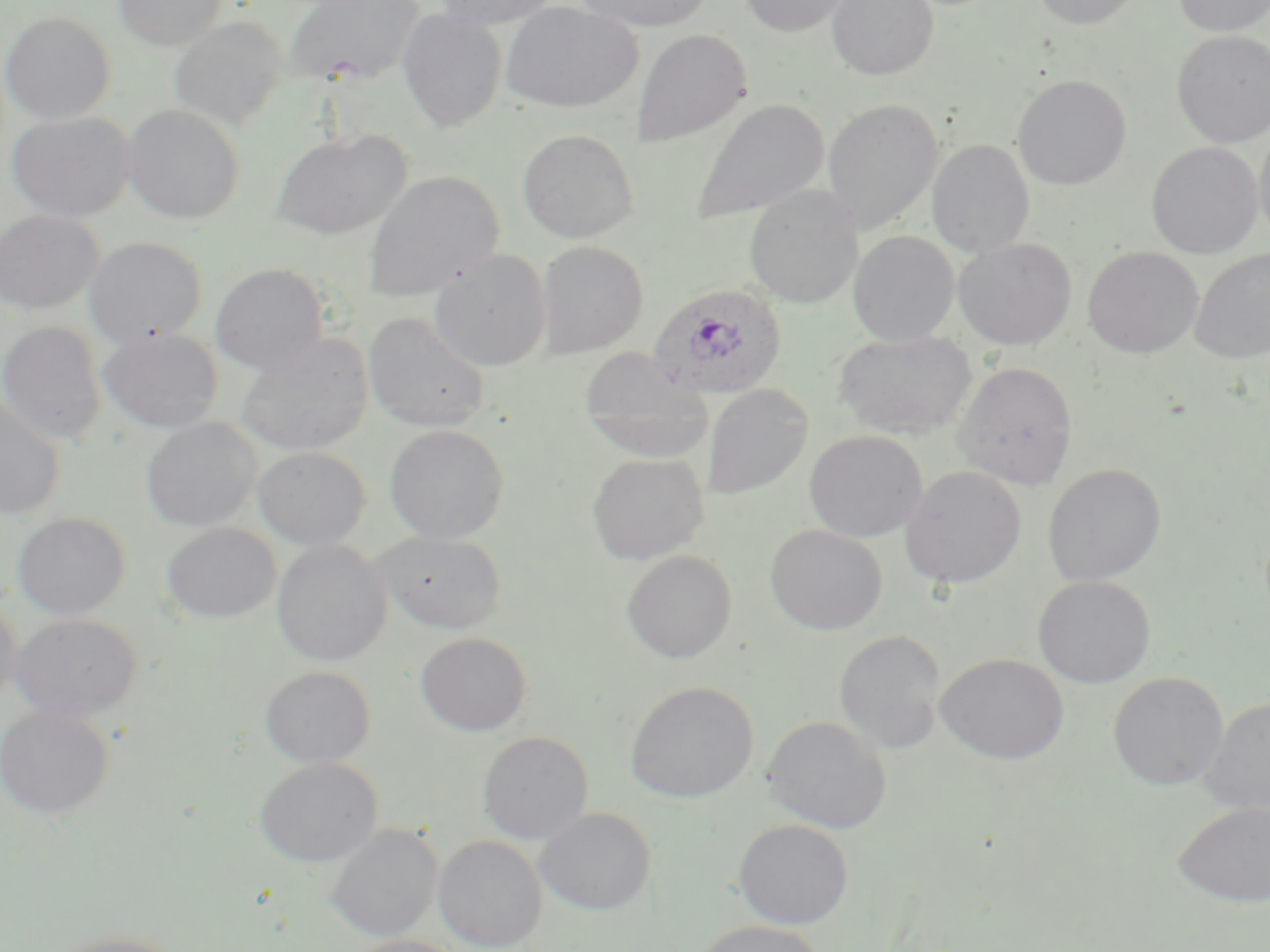

Summary:
  - Coordinate format: approximate bounding boxes as (x1, y1, x2, y2) in pixels
  - Plasmodium ovale-infected red blood cell locations: (648, 283, 788, 400)
  - Uninfected red blood cell locations: (113, 0, 227, 50), (283, 0, 426, 86), (434, 0, 564, 32), (573, 0, 716, 33), (740, 0, 851, 37), (826, 0, 939, 81), (1029, 0, 1143, 29), (1172, 0, 1270, 36), (500, 1, 642, 113), (396, 10, 507, 132), (1, 12, 115, 124), (169, 16, 287, 131), (631, 29, 751, 147), (1171, 30, 1270, 147), (1012, 74, 1132, 190), (823, 97, 944, 234), (690, 98, 830, 225), (121, 103, 245, 224), (5, 111, 136, 223), (1254, 123, 1270, 248), (517, 128, 639, 243), (271, 129, 412, 239), (927, 139, 1035, 257), (1146, 142, 1264, 259), (362, 169, 505, 302), (744, 186, 862, 309), (0, 210, 105, 315), (849, 231, 959, 347), (83, 236, 207, 348), (952, 237, 1078, 351), (537, 240, 648, 359), (1082, 246, 1204, 358), (1189, 247, 1270, 363), (429, 248, 551, 371), (210, 263, 329, 375), (363, 311, 491, 433), (0, 321, 107, 445), (98, 326, 223, 435), (833, 330, 978, 440), (236, 333, 373, 456), (579, 348, 712, 463), (953, 360, 1078, 489), (702, 384, 813, 500), (0, 395, 66, 521), (141, 416, 261, 532), (384, 424, 509, 543), (804, 430, 928, 543), (253, 446, 370, 550), (586, 453, 709, 565), (1043, 463, 1166, 587), (899, 465, 1026, 588), (12, 512, 131, 620), (161, 523, 280, 623), (765, 524, 888, 635), (372, 530, 508, 633), (271, 539, 392, 666), (621, 549, 737, 664), (1033, 575, 1156, 688), (0, 597, 22, 707), (9, 613, 142, 722), (834, 630, 946, 754), (415, 632, 532, 735), (935, 653, 1070, 765), (259, 666, 376, 768), (1108, 672, 1229, 791), (626, 680, 758, 804), (1199, 697, 1270, 815), (0, 705, 114, 819), (763, 715, 891, 833), (477, 731, 593, 845), (254, 757, 383, 867), (1173, 800, 1270, 907), (535, 807, 656, 915), (733, 819, 853, 929), (326, 824, 441, 942), (433, 835, 547, 952), (691, 920, 826, 952), (50, 931, 190, 952), (344, 934, 466, 952)
  - Slide-level diagnosis: Plasmodium ovale
  - Magnification: 1000x
  - Image size: 1270×952 pixels
  - Preparation: thin blood film
  - Field of view: one of a larger specimen
  - Stain: May-Grünwald-Giemsa
  - Modality: optical microscopy